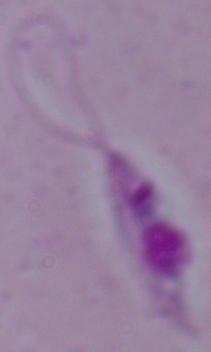
Summary:
  - Modality: photomicrograph
  - Identification: Leishmania
  - Magnification: 1000x